Name the blood parasite species.
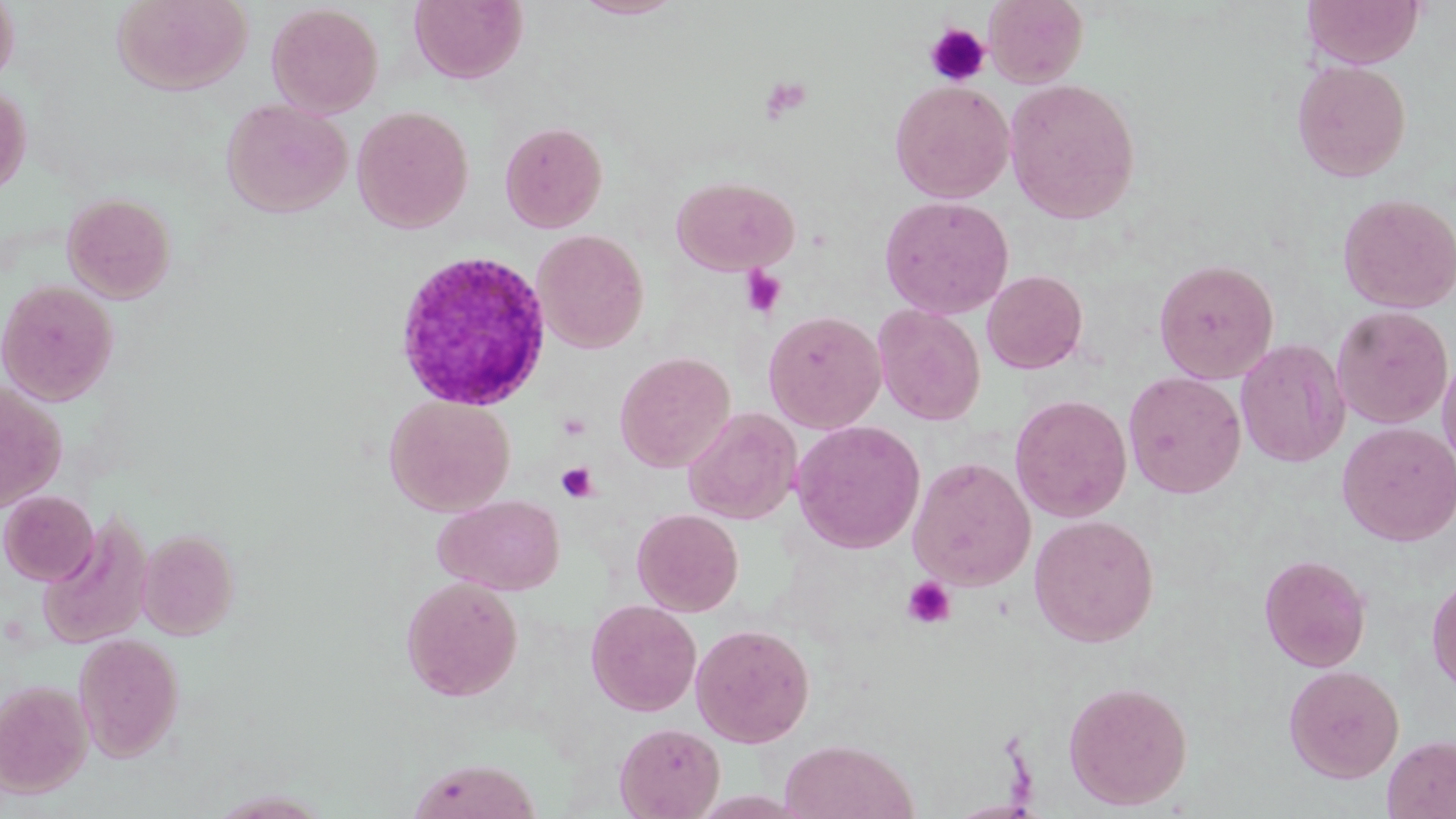
Plasmodium ovale.

{
  "image_size": "1456×819 pixels",
  "field_of_view": "single",
  "plasmodium_ovale_infected_red_blood_cell_locations": "approximate bounding boxes as (x1,y1)-(x2,y2) corner pairs in pixels: (391,248)-(552,412)",
  "uninfected_red_blood_cell_locations": "approximate bounding boxes as (x1,y1)-(x2,y2) corner pairs in pixels: (0,0)-(20,90), (112,0)-(252,95), (409,0)-(527,84), (572,0)-(685,20), (984,0)-(1088,88), (1302,0)-(1424,68), (266,3)-(384,119), (1291,59)-(1412,182), (1004,78)-(1141,223), (889,80)-(1015,204), (0,84)-(31,195), (221,98)-(353,218), (351,105)-(474,233), (499,120)-(608,233), (672,175)-(799,275), (62,192)-(176,303), (1337,192)-(1456,313), (878,195)-(1015,319), (532,229)-(649,354), (1153,258)-(1279,384), (982,270)-(1088,374), (0,279)-(119,405), (873,304)-(986,426), (1331,305)-(1453,429), (763,310)-(886,433), (1235,339)-(1350,468), (1437,350)-(1456,474), (614,351)-(736,473), (1123,371)-(1247,499), (0,380)-(67,513), (384,394)-(516,516), (1010,394)-(1132,523), (683,407)-(801,525), (790,420)-(926,554), (1337,422)-(1456,546), (908,456)-(1036,591), (1,490)-(98,585), (433,494)-(565,596), (632,508)-(744,616), (38,512)-(153,651), (1028,514)-(1159,647), (137,528)-(239,640), (1271,552)-(1382,780), (1259,553)-(1371,672), (1426,570)-(1456,697), (401,576)-(523,701), (586,599)-(702,716), (690,623)-(815,747), (74,633)-(184,761), (1283,664)-(1404,783), (0,679)-(93,797), (1063,680)-(1193,810), (615,721)-(725,819), (1382,735)-(1456,819), (778,739)-(919,819), (405,757)-(543,819), (206,790)-(333,818)",
  "magnification": "1000x",
  "stain": "May-Grünwald-Giemsa",
  "platelet_locations": "approximate bounding boxes as (x1,y1)-(x2,y2) corner pairs in pixels: (925,23)-(991,87), (759,76)-(813,121), (740,266)-(786,317), (556,462)-(600,502), (901,577)-(956,628)",
  "preparation": "thin blood film",
  "modality": "optical microscopy"
}